Classify this cell by malaria status.
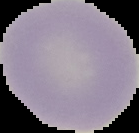
It is uninfected.

Summary:
  - Image size: 139×133 pixels
  - Preparation: thin blood smear
  - Image type: cell region segmented out of the field of view; surrounding area masked to black